Assess this cell for malaria.
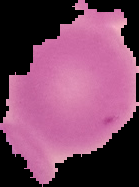

It is uninfected.

Image is 139×187 pixels. From a thin blood smear. Cell region segmented out of the field of view; the surrounding area is masked to black.